Describe the morphology of the erythrocytes.
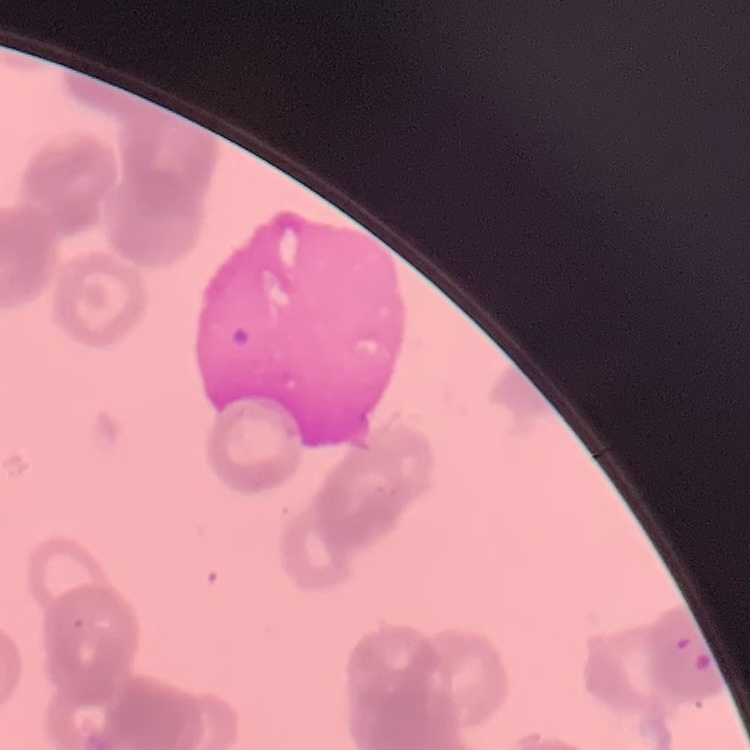
They show rouleaux formation.

Field's or Giemsa stain. One tile cut from a larger photomicrograph. Thin blood smear.